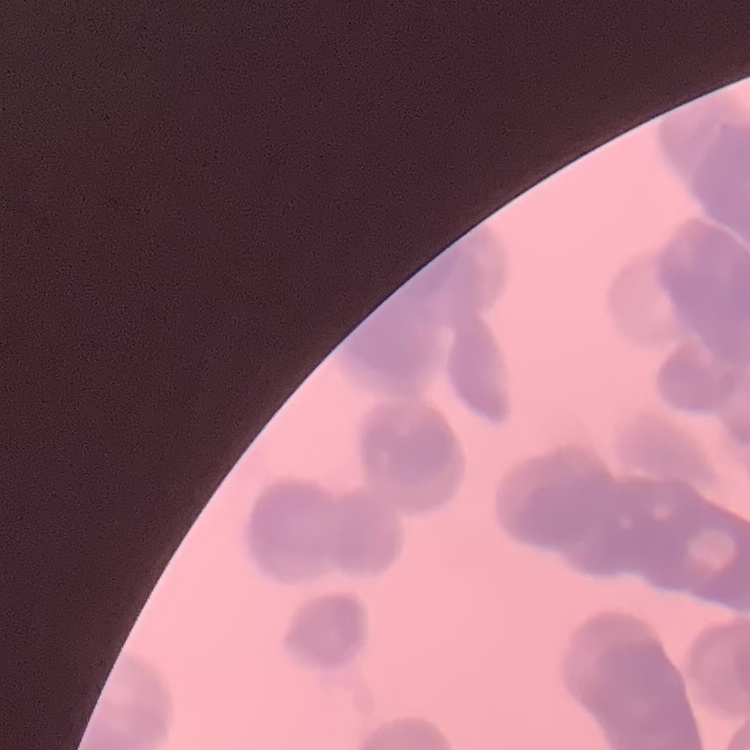

Summary:
  - Red blood cell morphology: rouleaux formation
  - Stain: Field's or Giemsa
  - Image type: one tile cut from a larger photomicrograph
  - Preparation: thin blood film